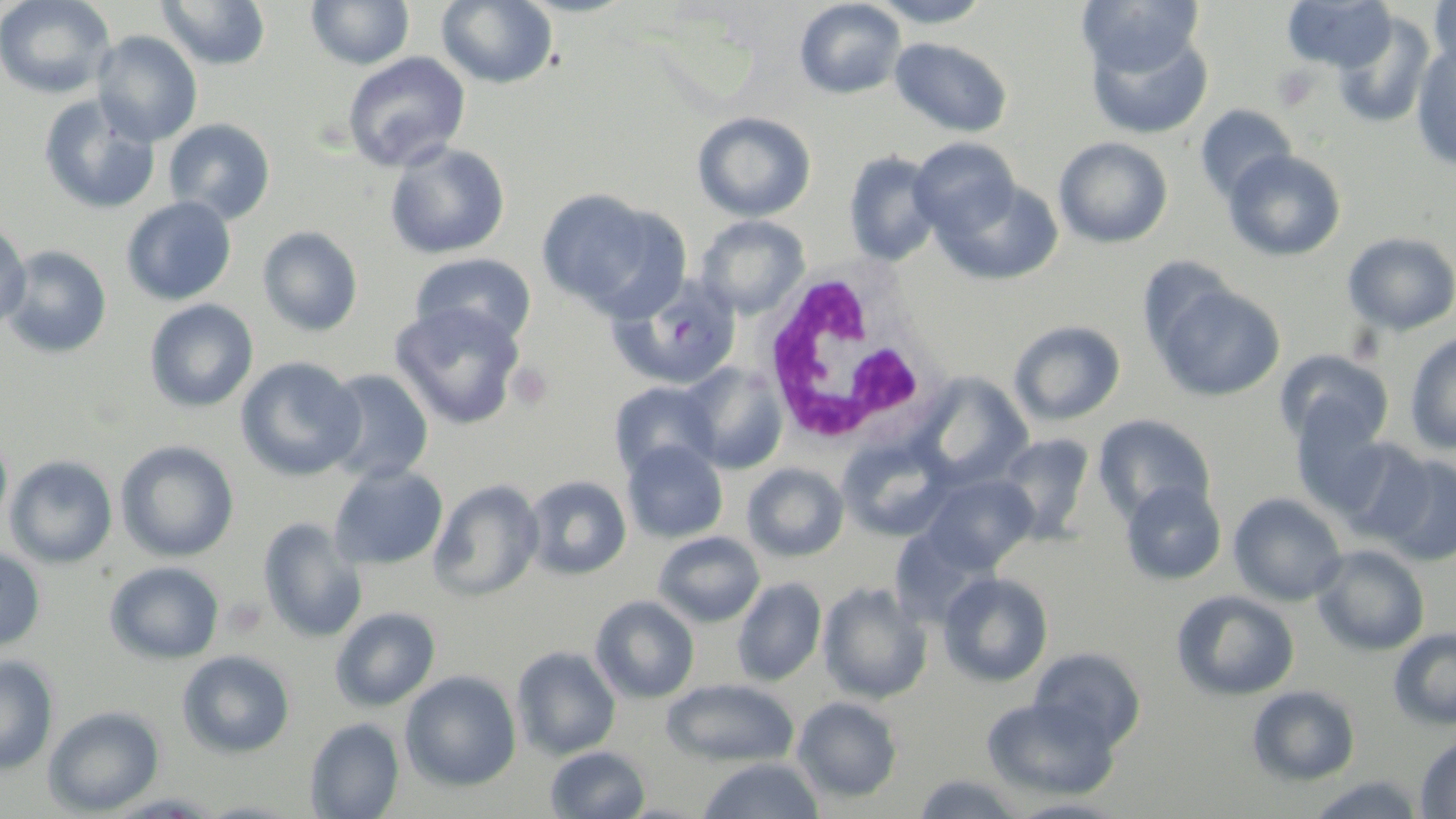 Approximate bounding boxes as (x1, y1, x2, y2) in pixels. Uninfected red blood cell locations: (0, 0, 116, 99), (156, 0, 272, 71), (305, 0, 416, 70), (437, 0, 559, 89), (794, 0, 906, 99), (865, 0, 994, 28), (1281, 0, 1396, 73), (1428, 0, 1456, 78), (1076, 1, 1206, 80), (1332, 12, 1436, 128), (1085, 24, 1213, 139), (92, 31, 203, 146), (889, 37, 1013, 138), (1411, 45, 1456, 170), (342, 51, 472, 172), (39, 93, 161, 215), (1195, 104, 1298, 202), (691, 111, 817, 222), (164, 118, 276, 225), (1053, 136, 1174, 248), (908, 137, 1020, 237), (384, 142, 511, 260), (1223, 149, 1346, 262), (842, 150, 944, 266), (934, 178, 1064, 286), (536, 187, 682, 316), (121, 196, 237, 306), (695, 215, 811, 320), (0, 220, 31, 329), (257, 226, 363, 337), (1342, 231, 1456, 336), (1, 245, 113, 359), (409, 252, 537, 346), (1136, 255, 1240, 365), (1153, 281, 1286, 402), (144, 299, 259, 413), (389, 302, 526, 431), (1008, 320, 1126, 426), (1404, 332, 1456, 455), (1274, 349, 1394, 451), (235, 356, 366, 482), (678, 362, 789, 475), (321, 368, 435, 485), (913, 373, 1035, 489), (607, 381, 720, 480), (1288, 402, 1393, 517), (1092, 414, 1216, 523), (0, 428, 13, 541), (993, 432, 1097, 542), (1334, 435, 1438, 544), (837, 437, 957, 542), (621, 439, 728, 543), (115, 440, 239, 563), (1372, 453, 1456, 566), (4, 455, 119, 569), (328, 463, 449, 571), (741, 463, 849, 562), (922, 472, 1038, 573), (523, 475, 633, 580), (1120, 479, 1227, 585), (428, 480, 545, 603), (1228, 492, 1347, 606), (257, 518, 368, 644), (887, 527, 990, 629), (653, 531, 765, 627), (1312, 544, 1431, 657), (0, 547, 47, 651), (104, 560, 225, 665), (937, 571, 1054, 687), (731, 577, 826, 687), (818, 581, 933, 703), (1170, 589, 1300, 701), (590, 594, 700, 704), (330, 606, 442, 711), (1387, 627, 1456, 730), (511, 645, 621, 760), (1028, 646, 1148, 750), (177, 649, 296, 758), (0, 654, 59, 775), (399, 670, 522, 791), (660, 677, 800, 766), (1247, 684, 1361, 786), (981, 695, 1120, 801), (791, 696, 903, 803), (43, 706, 165, 816), (304, 717, 405, 819), (1414, 732, 1456, 819), (544, 745, 651, 819), (695, 757, 827, 819), (910, 773, 1029, 818), (1303, 774, 1428, 819), (1005, 797, 1131, 819). White blood cell locations: (758, 263, 945, 448). Platelet locations: (1272, 66, 1320, 110), (507, 362, 553, 410), (220, 597, 268, 638). Plasmodium falciparum-infected red blood cell locations: (611, 275, 743, 390). Slide-level diagnosis: Plasmodium falciparum. Thin blood smear. Single field of view. May-Grünwald-Giemsa stain. Light microscopy. Captured at 1000x magnification. Image is 1456×819 pixels.